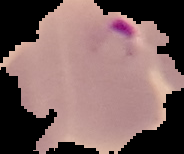

Segmented cell region on a black background. Malaria status: parasitized. From a thin blood film. Image is 184×154 pixels.